Locate every blood parasite and identify its species.
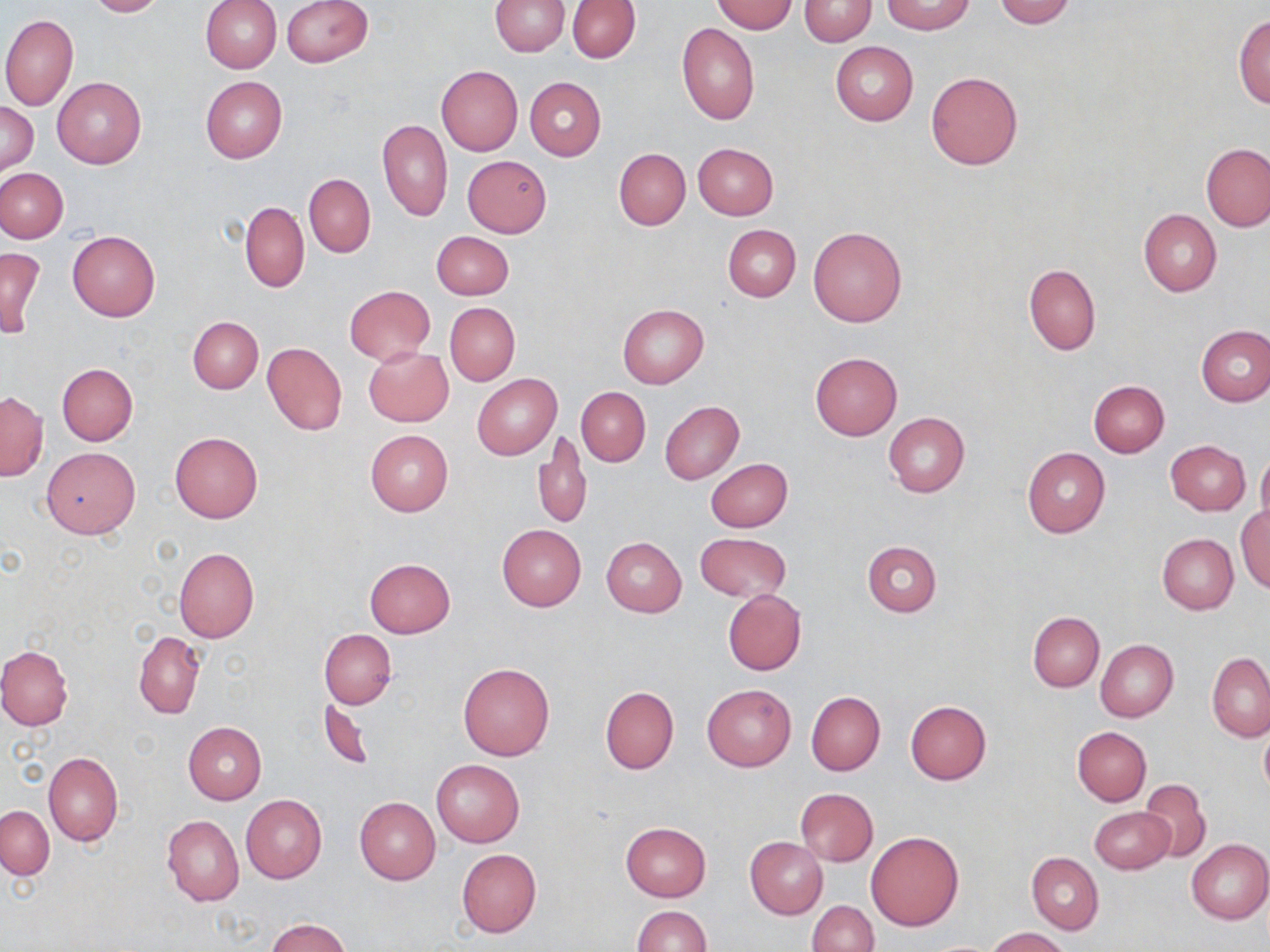
No blood parasites observed.

Summary:
  - Coordinate format: approximate bounding boxes as (x1, y1, x2, y2) in pixels
  - Uninfected red blood cell locations: (84, 0, 164, 17), (202, 0, 282, 73), (280, 0, 373, 66), (489, 0, 570, 56), (567, 0, 640, 63), (994, 0, 1076, 27), (710, 1, 797, 33), (799, 1, 876, 45), (882, 1, 975, 34), (1, 14, 78, 110), (1234, 14, 1270, 107), (677, 22, 760, 125), (830, 42, 918, 125), (436, 66, 523, 155), (926, 72, 1022, 170), (199, 76, 287, 163), (52, 77, 146, 168), (525, 77, 606, 160), (0, 102, 39, 174), (378, 119, 452, 222), (691, 142, 779, 220), (1201, 143, 1269, 231), (614, 148, 691, 230), (462, 154, 552, 238), (1, 168, 68, 243), (304, 174, 376, 257), (241, 202, 309, 293), (1138, 209, 1221, 296), (723, 225, 801, 301), (808, 227, 907, 327), (67, 231, 160, 321), (433, 232, 513, 299), (0, 247, 44, 338), (1024, 264, 1100, 355), (344, 285, 435, 364), (445, 303, 519, 385), (617, 304, 709, 388), (188, 316, 262, 393), (185, 322, 333, 404), (1196, 326, 1270, 407), (262, 342, 347, 436), (364, 346, 454, 426), (810, 352, 902, 439), (56, 363, 138, 446), (472, 374, 561, 459), (1088, 380, 1170, 456), (576, 387, 651, 467), (0, 391, 47, 481), (660, 401, 744, 484), (883, 411, 970, 497), (365, 430, 453, 516), (534, 431, 590, 531), (170, 432, 264, 523), (1166, 440, 1250, 516), (42, 447, 140, 538), (1022, 447, 1110, 538), (1257, 452, 1270, 531), (705, 458, 793, 532), (1236, 504, 1270, 593), (497, 524, 586, 611), (694, 533, 791, 602), (1157, 533, 1238, 613), (601, 536, 687, 616), (861, 540, 942, 616), (174, 547, 259, 642), (363, 559, 455, 638), (723, 589, 807, 675), (1028, 611, 1104, 692), (320, 629, 395, 709), (134, 631, 204, 718), (1095, 639, 1178, 722), (0, 646, 74, 731), (1207, 653, 1270, 741), (458, 662, 554, 760), (702, 684, 796, 771), (600, 686, 679, 773), (806, 691, 885, 775), (319, 700, 374, 770), (905, 700, 991, 784), (184, 722, 265, 805), (1259, 724, 1270, 797), (1074, 727, 1151, 806), (44, 751, 123, 847), (432, 760, 525, 847), (1138, 779, 1212, 863), (795, 788, 878, 866), (240, 794, 327, 883), (354, 797, 440, 884), (0, 806, 53, 879), (1089, 806, 1175, 875), (162, 814, 243, 907), (620, 822, 711, 902), (866, 831, 963, 930), (746, 837, 828, 918), (1186, 839, 1270, 924), (456, 849, 541, 937), (1028, 853, 1103, 934), (808, 901, 879, 952), (631, 905, 712, 951), (265, 917, 353, 952), (985, 927, 1071, 951)
  - Slide-level diagnosis: negative for blood parasites
  - Modality: light microscopy
  - Field of view: one of a larger specimen
  - Preparation: thin blood film
  - Image size: 1270×952 pixels
  - Magnification: 1000x
  - Stain: May-Grünwald-Giemsa